Name the parasite shown.
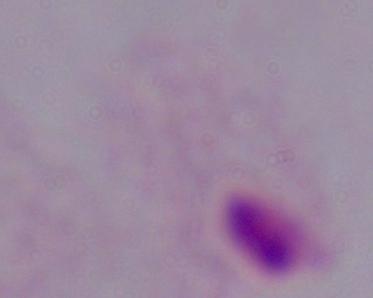
A trichomonad.

Summary:
  - Magnification: 1000x
  - Modality: photomicrograph